Outline each blood parasite and name the species.
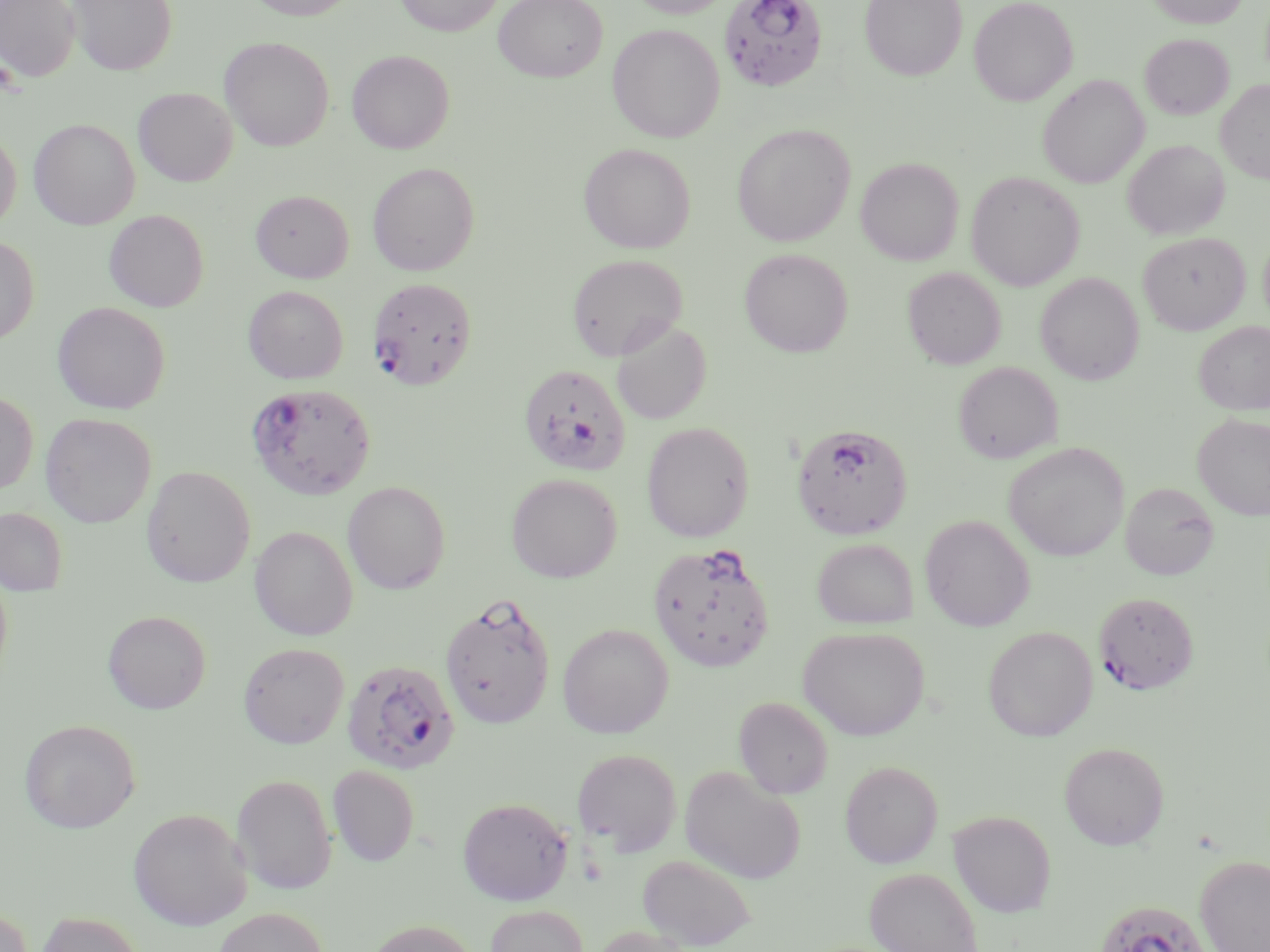

Approximate bounding boxes as (x1, y1, x2, y2) in pixels.
Plasmodium falciparum-infected red blood cells: (718, 0, 829, 92), (368, 277, 478, 390), (518, 363, 631, 476), (246, 382, 377, 500), (792, 423, 914, 540), (648, 542, 776, 672), (1094, 592, 1199, 695), (440, 593, 555, 729), (341, 659, 460, 775), (1095, 899, 1210, 952).
No Plasmodium ovale, Plasmodium malariae, Plasmodium vivax, Babesia divergens, or Trypanosoma brucei observed.

Summary:
  - Uninfected red blood cell locations: (0, 0, 81, 81), (67, 0, 177, 75), (245, 0, 359, 20), (394, 0, 505, 36), (494, 0, 608, 82), (627, 0, 735, 18), (860, 0, 967, 81), (968, 0, 1078, 106), (1147, 0, 1248, 28), (607, 23, 725, 142), (1140, 33, 1234, 119), (220, 37, 334, 151), (347, 50, 454, 153), (1037, 74, 1149, 188), (1216, 80, 1270, 185), (133, 87, 237, 186), (29, 118, 140, 229), (732, 123, 855, 246), (0, 128, 21, 232), (1122, 140, 1229, 240), (578, 142, 695, 254), (856, 157, 964, 265), (368, 162, 479, 276), (966, 171, 1085, 290), (251, 190, 354, 283), (104, 209, 209, 311), (1259, 231, 1270, 330), (1138, 232, 1250, 334), (0, 235, 39, 345), (739, 248, 853, 357), (567, 253, 688, 361), (903, 267, 1006, 369), (1035, 272, 1144, 385), (243, 285, 348, 384), (52, 301, 171, 414), (612, 319, 712, 424), (1195, 321, 1270, 415), (953, 361, 1062, 464), (0, 391, 38, 496), (40, 413, 156, 528), (1193, 413, 1270, 520), (641, 422, 755, 543), (1003, 442, 1129, 562), (141, 465, 256, 587), (507, 473, 623, 582), (343, 481, 450, 594), (1120, 482, 1219, 580), (0, 507, 68, 595), (920, 514, 1035, 631), (250, 525, 358, 641), (812, 538, 919, 629), (0, 566, 13, 689), (103, 610, 210, 714), (557, 623, 673, 738), (798, 626, 929, 740), (983, 626, 1097, 741), (238, 643, 349, 748), (734, 697, 833, 799), (19, 719, 140, 833), (1059, 741, 1169, 850), (572, 748, 682, 855), (840, 760, 943, 868), (328, 765, 419, 866), (679, 765, 806, 885), (231, 774, 337, 894), (458, 797, 573, 905), (128, 807, 252, 931), (948, 810, 1056, 917), (638, 854, 756, 951), (1196, 856, 1270, 952), (864, 867, 983, 952), (485, 904, 589, 952), (0, 907, 33, 952), (211, 907, 330, 952), (33, 912, 146, 952), (363, 919, 481, 952), (590, 925, 696, 952)
  - Slide-level diagnosis: Plasmodium falciparum
  - Field of view: one of a larger specimen
  - Magnification: 1000x
  - Preparation: thin blood smear
  - Modality: optical microscopy
  - Stain: May-Grünwald-Giemsa
  - Image size: 1270×952 pixels